Report the malaria status of this cell.
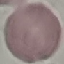

Uninfected.

Summary:
  - Stain: Giemsa
  - Image type: cell patch, automatically extracted from a larger field of view and resized to 64 × 64 pixels
  - Capture: smartphone through the microscope eyepiece
  - Preparation: thin blood film